Describe the morphology of the erythrocytes.
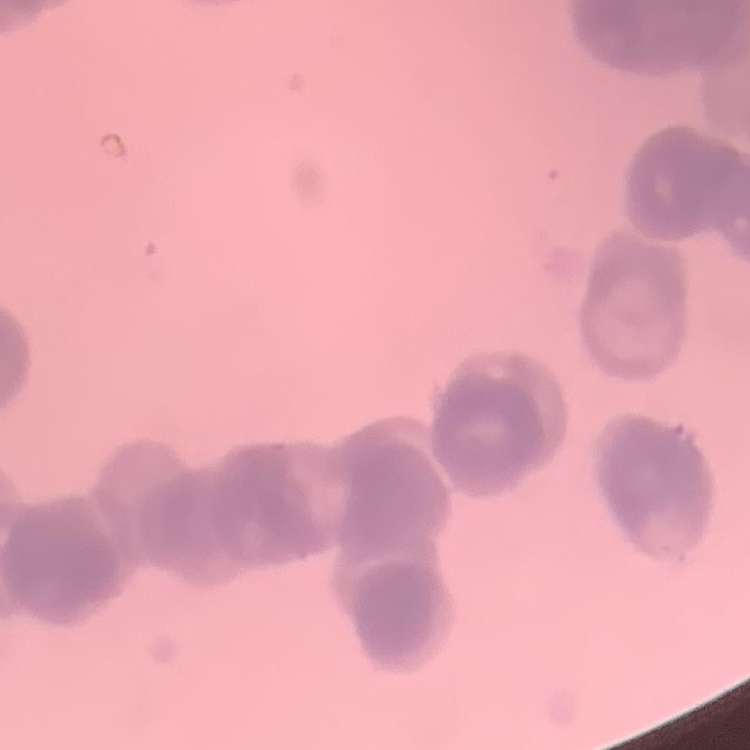
Rouleaux formation.

Summary:
  - Stain: Field's or Giemsa
  - Preparation: thin blood smear
  - Image type: one tile cut from a larger photomicrograph